Locate every Plasmodium falciparum parasite and give its life-cycle stage, and locate every leukocyte and any debris.
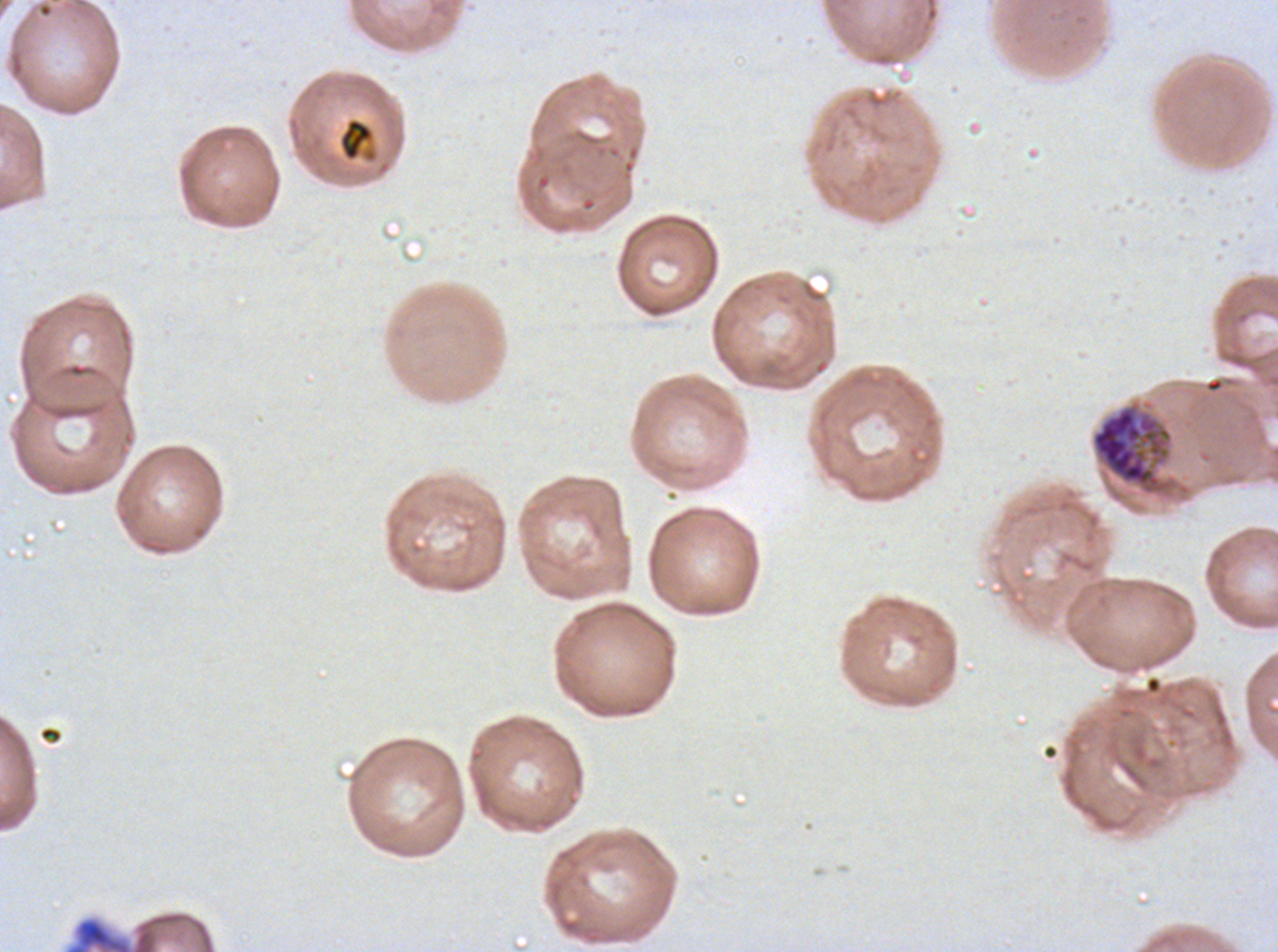

Approximate bounding boxes as {x1, y1, x2, y2} in pixels.
Early schizonts: {1090, 404, 1173, 495}.
Debris: {338, 116, 378, 164}, {69, 918, 132, 951}.
No rings, late-ring/early-trophozoite forms, mid trophozoites, late trophozoites, late schizonts, segmenters, gametocytes, or leukocytes observed.

Image is 1278×952 pixels. Giemsa stain. Thin blood film. One sub-image of a larger composite. Plasmodium falciparum from a patient in The Gambia, cultured ex vivo for 24 to 48 hours.